Classify this cell by malaria status.
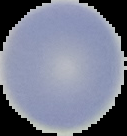
It is uninfected.

preparation = thin blood smear
image size = 127×136 pixels
image type = cell region segmented out of the field of view; surrounding area masked to black